Locate platelets.
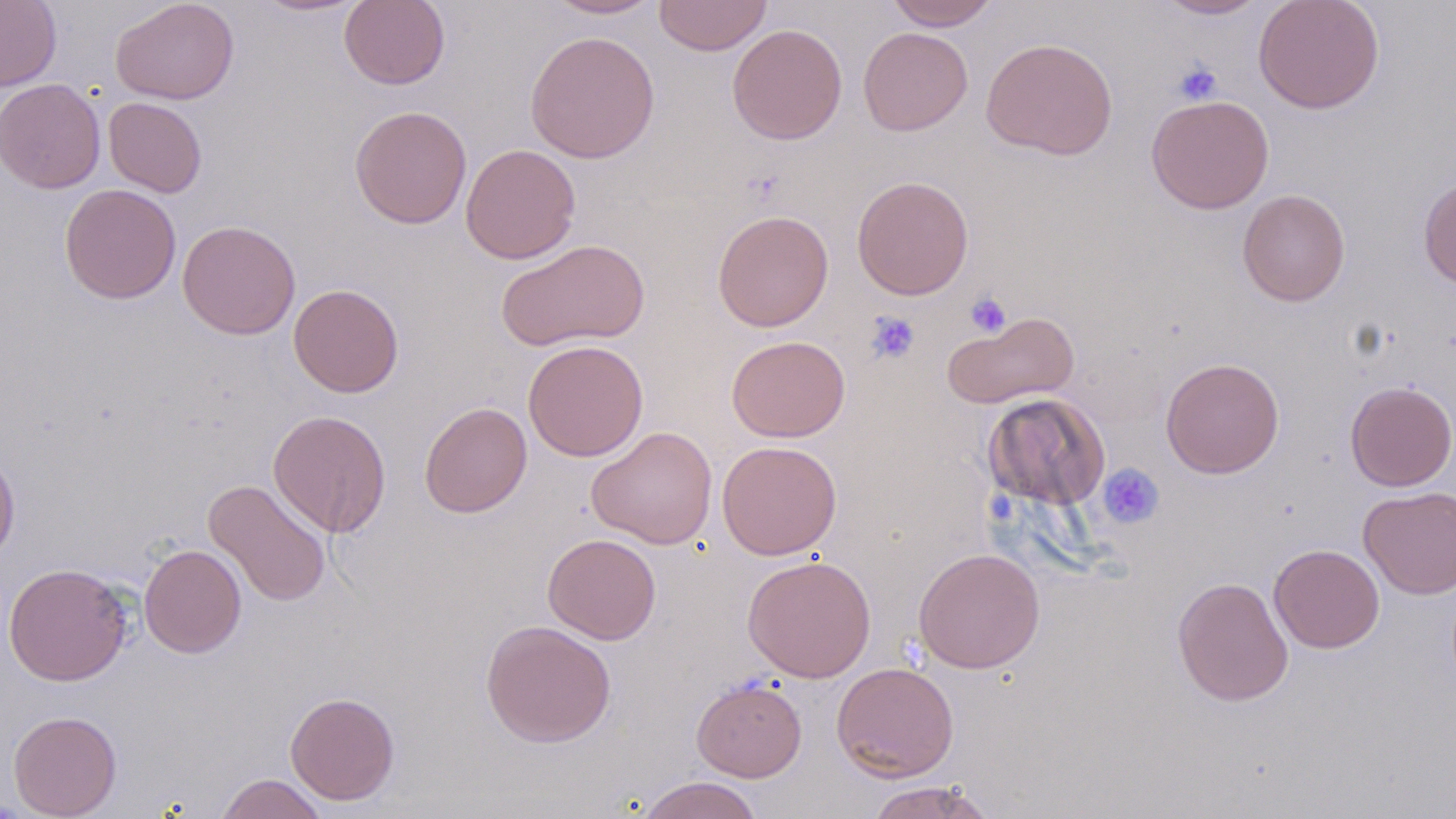

Approximate bounding boxes as named x1/y1/x2/y2 corners in pixels.
Platelets: (x1=1172, y1=60, x2=1223, y2=105), (x1=966, y1=291, x2=1011, y2=337), (x1=866, y1=311, x2=921, y2=364), (x1=1098, y1=463, x2=1164, y2=529).

Summary:
  - Uninfected red blood cell locations: (x1=0, y1=0, x2=61, y2=91), (x1=110, y1=0, x2=240, y2=105), (x1=253, y1=0, x2=369, y2=17), (x1=339, y1=0, x2=450, y2=90), (x1=545, y1=0, x2=662, y2=19), (x1=653, y1=0, x2=772, y2=56), (x1=885, y1=0, x2=1000, y2=30), (x1=1153, y1=0, x2=1269, y2=20), (x1=1253, y1=0, x2=1385, y2=114), (x1=727, y1=23, x2=847, y2=145), (x1=858, y1=27, x2=973, y2=135), (x1=524, y1=30, x2=660, y2=164), (x1=981, y1=37, x2=1118, y2=160), (x1=1, y1=78, x2=106, y2=194), (x1=1146, y1=94, x2=1274, y2=214), (x1=103, y1=97, x2=207, y2=197), (x1=349, y1=104, x2=472, y2=229), (x1=461, y1=143, x2=581, y2=264), (x1=1418, y1=174, x2=1456, y2=290), (x1=851, y1=175, x2=975, y2=300), (x1=59, y1=185, x2=181, y2=304), (x1=1237, y1=188, x2=1351, y2=307), (x1=712, y1=209, x2=834, y2=332), (x1=177, y1=220, x2=301, y2=340), (x1=497, y1=238, x2=650, y2=351), (x1=288, y1=283, x2=404, y2=397), (x1=943, y1=310, x2=1079, y2=409), (x1=726, y1=335, x2=850, y2=442), (x1=522, y1=340, x2=649, y2=461), (x1=1160, y1=357, x2=1285, y2=478), (x1=1344, y1=380, x2=1456, y2=491), (x1=983, y1=393, x2=1109, y2=510), (x1=419, y1=401, x2=532, y2=517), (x1=267, y1=409, x2=392, y2=537), (x1=587, y1=426, x2=717, y2=549), (x1=716, y1=440, x2=842, y2=560), (x1=0, y1=448, x2=20, y2=564), (x1=203, y1=478, x2=332, y2=607), (x1=1358, y1=486, x2=1455, y2=599), (x1=542, y1=533, x2=662, y2=644), (x1=139, y1=543, x2=246, y2=658), (x1=1269, y1=544, x2=1384, y2=653), (x1=913, y1=547, x2=1045, y2=674), (x1=741, y1=555, x2=876, y2=682), (x1=3, y1=562, x2=133, y2=686), (x1=1171, y1=576, x2=1294, y2=707), (x1=480, y1=619, x2=616, y2=748), (x1=831, y1=661, x2=960, y2=782), (x1=691, y1=677, x2=807, y2=782), (x1=285, y1=691, x2=400, y2=805), (x1=8, y1=710, x2=122, y2=818), (x1=215, y1=773, x2=328, y2=819), (x1=634, y1=775, x2=765, y2=819), (x1=864, y1=780, x2=997, y2=819)
  - Slide-level diagnosis: negative for blood parasites
  - Field of view: one of a larger specimen
  - Magnification: 1000x
  - Preparation: thin blood smear
  - Modality: light microscopy
  - Image size: 1456×819 pixels
  - Stain: May-Grünwald-Giemsa